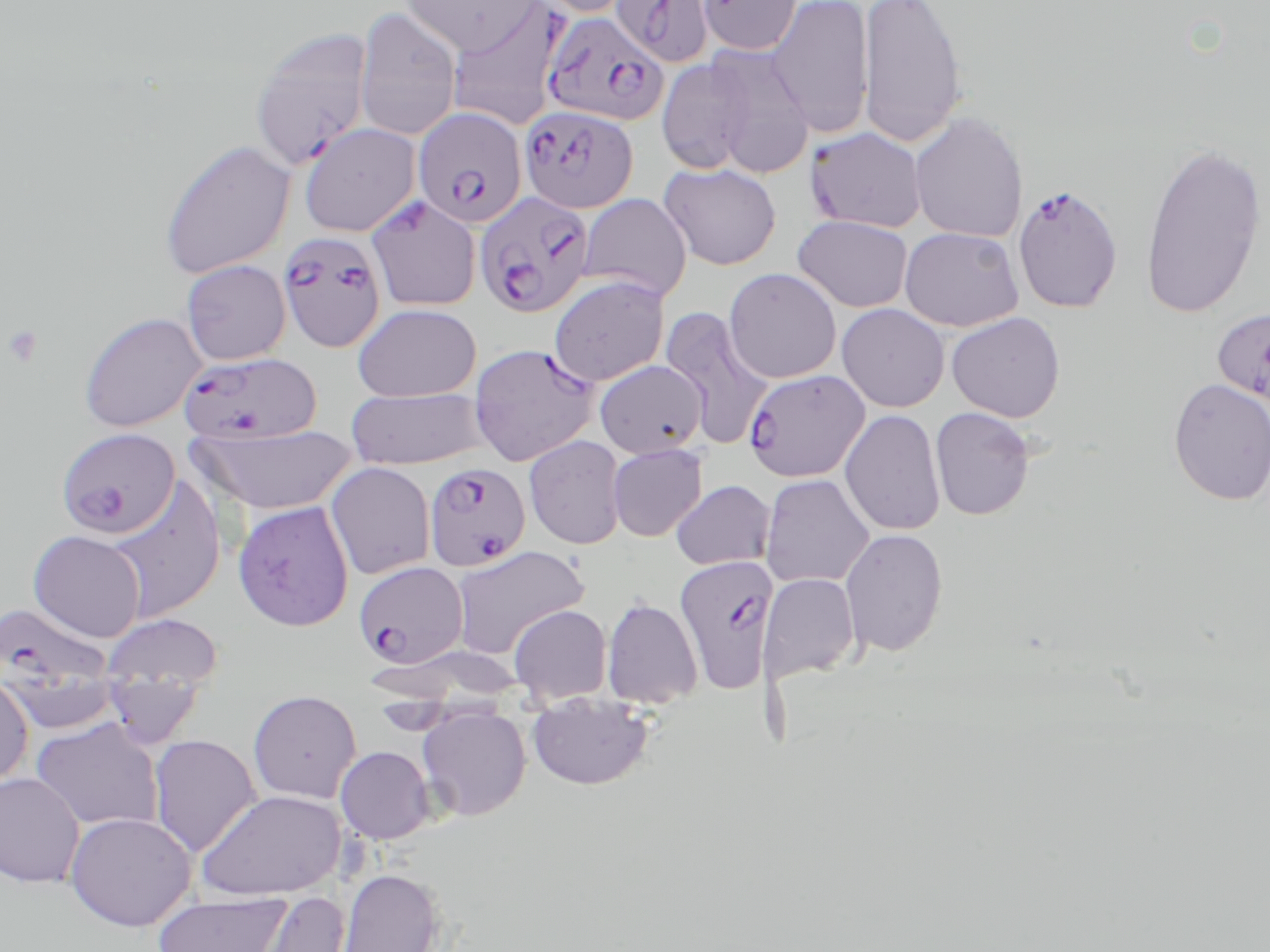
Approximate bounding boxes as (x1,y1)-(x2,y2) corner pairs in pixels. Platelet locations: (2,325)-(43,368). Plasmodium falciparum-infected red blood cell locations (subset): (611,0)-(715,68), (696,0)-(803,56), (445,2)-(566,131), (542,11)-(671,127), (248,26)-(375,171), (520,105)-(639,214), (413,106)-(528,229), (805,126)-(928,234), (473,191)-(595,319), (364,195)-(481,311), (278,230)-(387,353), (1211,307)-(1270,410), (469,343)-(600,466), (178,352)-(320,445), (743,369)-(869,483), (424,462)-(532,572), (673,555)-(781,692), (353,560)-(469,668), (1,600)-(114,693). Uninfected red blood cell locations (subset): (401,0)-(541,55), (529,0)-(637,18), (766,0)-(875,137), (858,0)-(969,149), (354,5)-(463,141), (684,44)-(815,177), (655,55)-(763,175), (908,112)-(1029,243), (298,122)-(421,237), (157,138)-(296,280), (1139,139)-(1268,319), (659,162)-(782,270), (577,193)-(692,302), (792,215)-(914,312), (899,226)-(1024,331), (181,260)-(291,367), (723,267)-(842,383), (548,275)-(671,386), (352,303)-(482,401), (836,303)-(949,412), (659,308)-(773,450), (77,311)-(207,433), (945,311)-(1066,422), (594,360)-(707,457), (1167,377)-(1270,505), (346,386)-(491,469), (929,406)-(1036,520), (839,409)-(946,536), (190,425)-(358,514), (55,427)-(181,539), (523,435)-(627,550), (607,443)-(708,542), (325,461)-(436,580), (759,474)-(875,588), (107,479)-(227,623), (670,480)-(776,570), (232,500)-(355,632), (839,526)-(949,657), (28,530)-(146,642), (448,546)-(589,658), (758,573)-(861,682), (600,597)-(704,709), (508,604)-(613,706), (99,612)-(225,689), (364,644)-(534,704), (0,672)-(34,790), (102,677)-(206,746), (247,689)-(362,804), (527,696)-(655,791), (416,706)-(532,821), (30,717)-(164,832), (148,734)-(262,856), (335,745)-(436,844), (0,771)-(87,888), (197,788)-(347,901), (64,810)-(197,931), (335,867)-(447,952), (244,891)-(351,952), (152,892)-(293,952). Slide-level diagnosis: Plasmodium falciparum. Thin blood smear. Captured at 1000x magnification. May-Grünwald-Giemsa-stained preparation. Optical microscopy. One field of a larger specimen. Image is 1270×952 pixels.